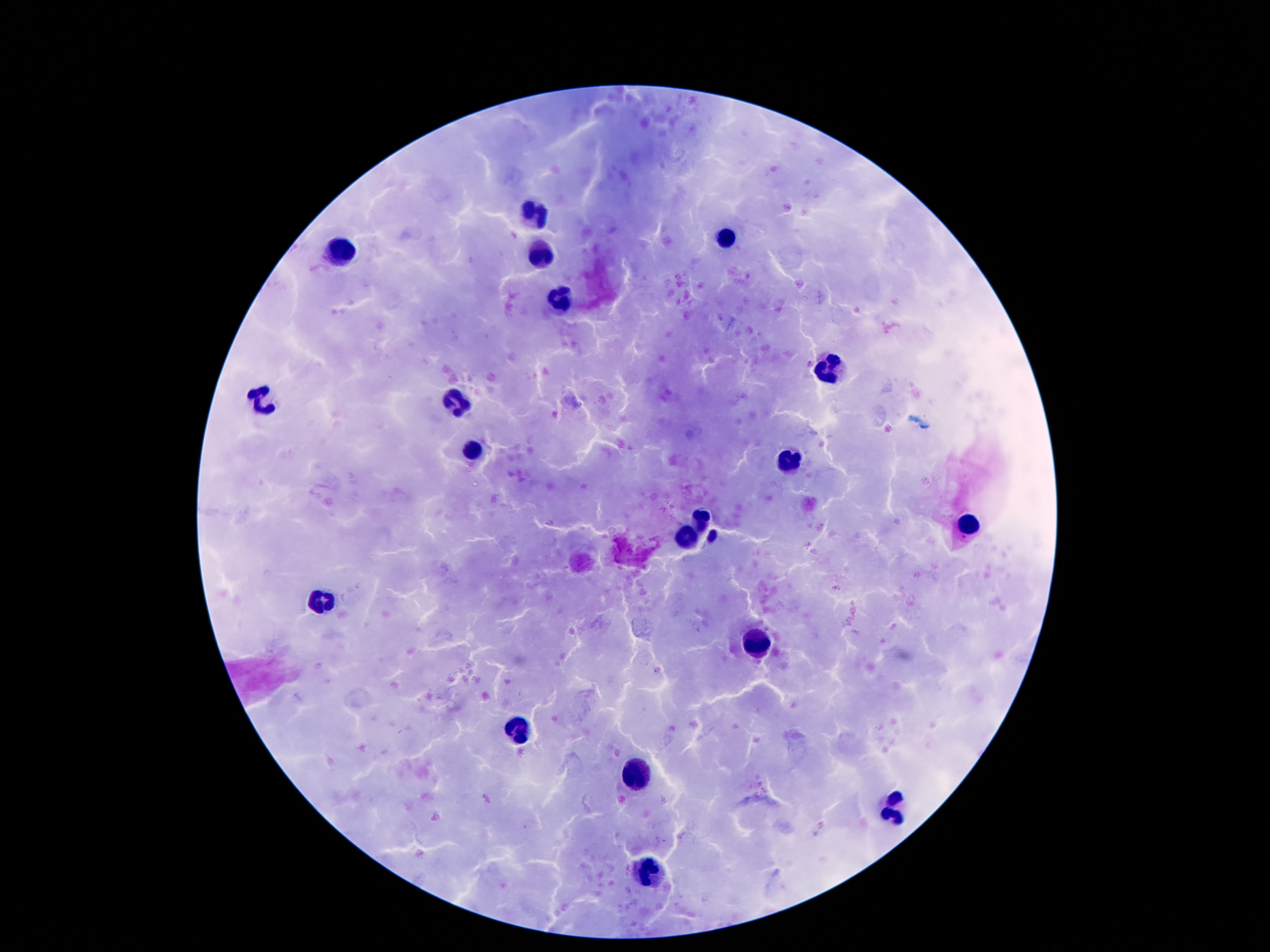

Approximate centers as [x, y] in pixels.
Summary:
  - Leukocyte locations: [535, 218], [727, 237], [539, 250], [341, 252], [559, 297], [829, 370], [263, 398], [455, 404], [471, 452], [789, 462], [705, 514], [971, 525], [687, 534], [325, 602], [761, 642], [515, 725], [637, 772], [895, 811], [647, 874]
  - Preparation: thick blood film
  - Stain: Giemsa
  - Capture: smartphone camera through the microscope eyepiece
  - Patient malaria status: not infected
  - Image size: 1270×952 pixels
  - Field of view: single
  - Magnification: 100x